Comment on the morphology of the red blood cells.
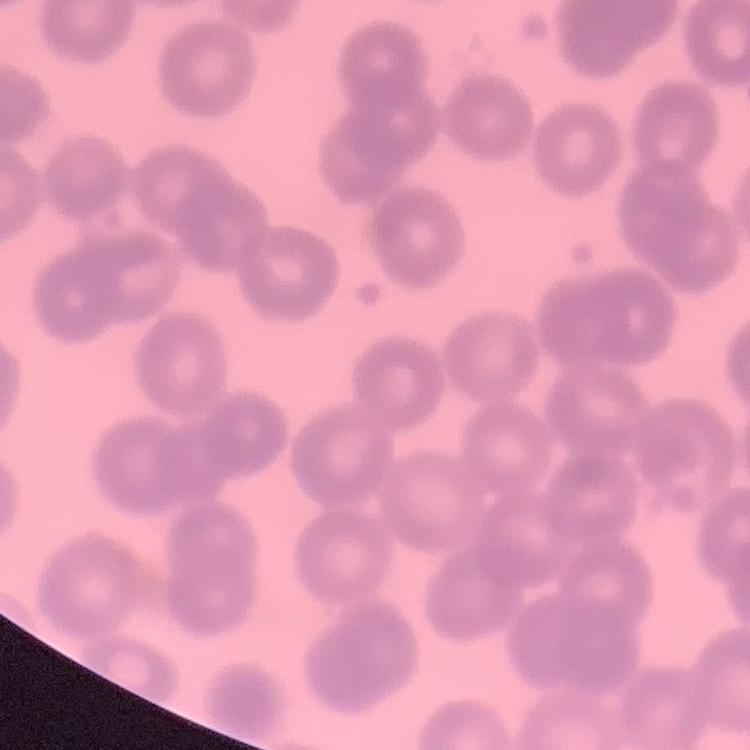

They show no rouleaux formation.

Summary:
  - Image type: square crop of a larger photomicrograph
  - Stain: Field's or Giemsa
  - Preparation: thin blood film